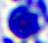 Micrograph. 400x magnification. A white blood cell is seen.